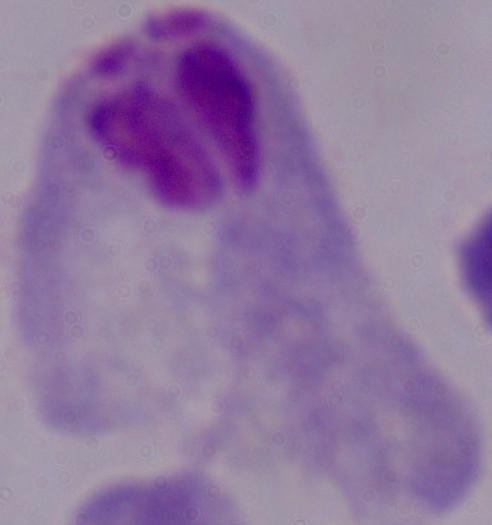
Summary:
  - Modality: micrograph
  - Identification: trichomonad
  - Magnification: 1000x